Assess the morphology of the red blood cells.
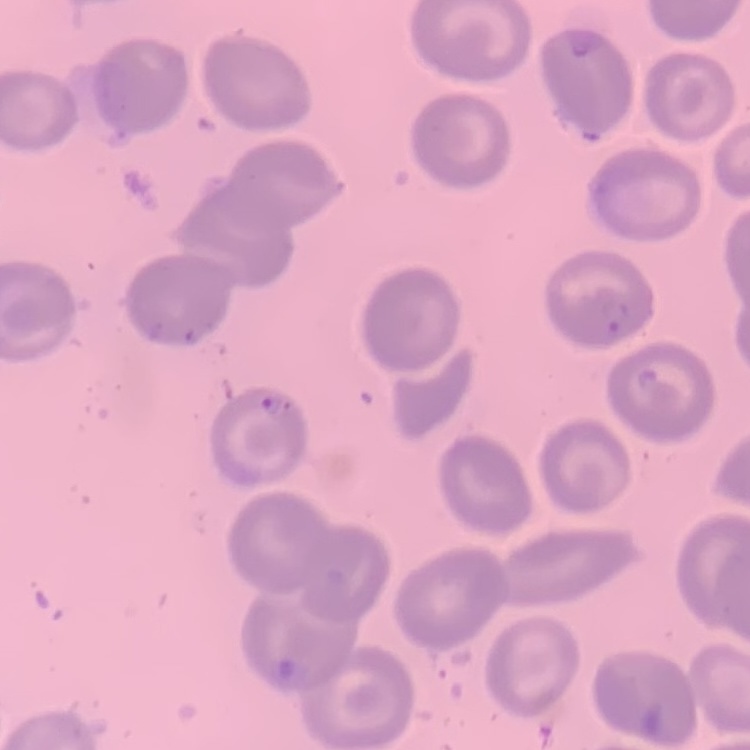
They show no rouleaux formation.

Summary:
  - Image type: square crop of a larger photomicrograph
  - Preparation: thin blood film
  - Stain: Field's or Giemsa